Report the malaria status of this cell.
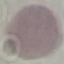
It is uninfected.

Summary:
  - Image type: automatically extracted cell patch, resized to 64 × 64 pixels
  - Stain: Giemsa
  - Preparation: thin blood film
  - Capture: smartphone through the microscope eyepiece